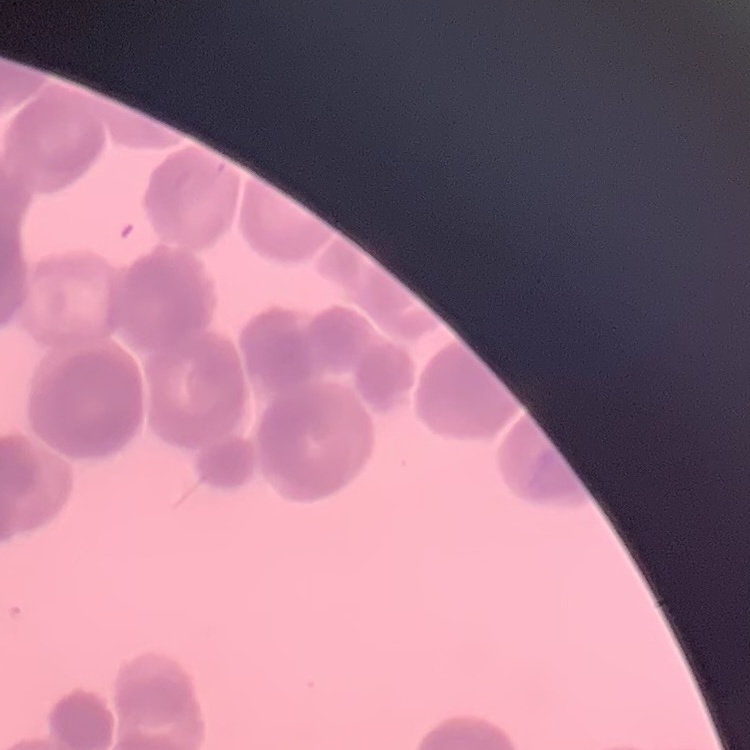

Summary:
  - Red blood cell morphology: rouleaux formation
  - Stain: Field's or Giemsa
  - Preparation: thin blood smear
  - Image type: square crop of a larger photomicrograph